State the blood parasite species.
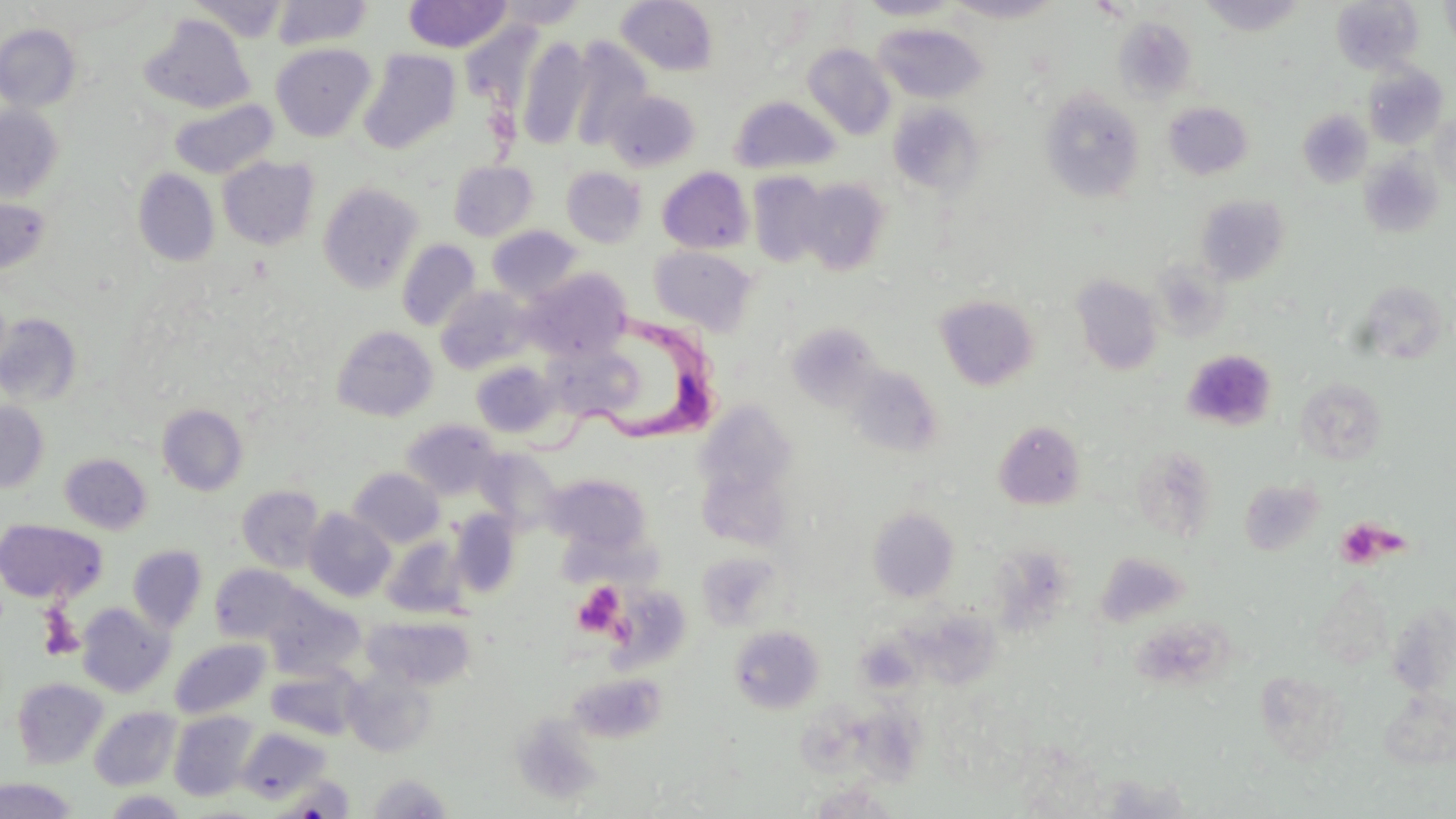
Trypanosoma brucei.

Approximate bounding boxes as (x1,y1)-(x2,y2) corner pairs in pixels. Uninfected red blood cell locations: (188,0)-(289,42), (271,0)-(373,50), (402,0)-(513,53), (616,0)-(718,76), (857,0)-(965,20), (946,0)-(1065,23), (1198,0)-(1308,36), (1440,0)-(1456,53), (493,1)-(589,29), (1330,1)-(1423,74), (140,14)-(254,114), (1113,17)-(1197,102), (0,23)-(81,112), (873,23)-(987,103), (515,35)-(594,149), (567,38)-(653,149), (271,43)-(376,141), (802,44)-(896,140), (358,49)-(460,154), (1363,63)-(1450,149), (1040,88)-(1145,203), (605,90)-(701,172), (730,97)-(840,175), (170,99)-(277,178), (1163,101)-(1253,180), (888,103)-(983,196), (0,104)-(64,204), (1297,110)-(1372,187), (1430,112)-(1456,190), (1358,155)-(1443,237), (218,156)-(319,250), (449,161)-(538,241), (561,167)-(647,248), (657,167)-(754,255), (133,169)-(219,267), (748,173)-(832,269), (794,177)-(891,276), (318,181)-(424,294), (1195,195)-(1290,286), (0,196)-(51,276), (487,226)-(582,302), (397,239)-(481,332), (650,246)-(758,336), (1153,262)-(1230,338), (525,269)-(631,362), (1072,274)-(1164,375), (1356,280)-(1451,365), (435,287)-(534,375), (935,294)-(1039,391), (0,313)-(81,407), (787,323)-(881,410), (332,325)-(438,421), (543,341)-(641,423), (471,361)-(560,438), (846,365)-(944,459), (1295,376)-(1388,466), (0,400)-(50,493), (158,404)-(248,495), (402,419)-(500,500), (994,420)-(1087,510), (474,447)-(562,533), (59,453)-(152,534), (348,467)-(444,547), (543,472)-(653,559), (237,485)-(324,572), (868,506)-(959,603), (304,508)-(395,602), (449,511)-(521,598), (0,519)-(105,604), (382,537)-(468,619), (128,545)-(207,633), (696,552)-(782,631), (210,564)-(308,645), (263,591)-(364,679), (77,603)-(174,696), (365,616)-(476,690), (730,626)-(823,713), (170,639)-(270,719), (267,666)-(362,740), (343,667)-(438,757), (567,672)-(665,743), (13,677)-(108,769), (1379,690)-(1455,769), (89,706)-(181,791), (169,710)-(260,801), (510,714)-(604,806), (236,725)-(333,805), (366,773)-(452,818), (1082,773)-(1202,818), (275,775)-(356,817), (0,777)-(77,818), (804,782)-(905,818), (102,790)-(190,818). Trypanosoma brucei locations: (523,305)-(724,471). Platelet locations: (1182,349)-(1277,432), (1335,517)-(1398,569), (573,582)-(625,636). Image is 1456×819 pixels. May-Grünwald-Giemsa stain. Light microscopy. Single field of view. 1000x magnification. Thin blood film.